Evaluate for Plasmodium parasites.
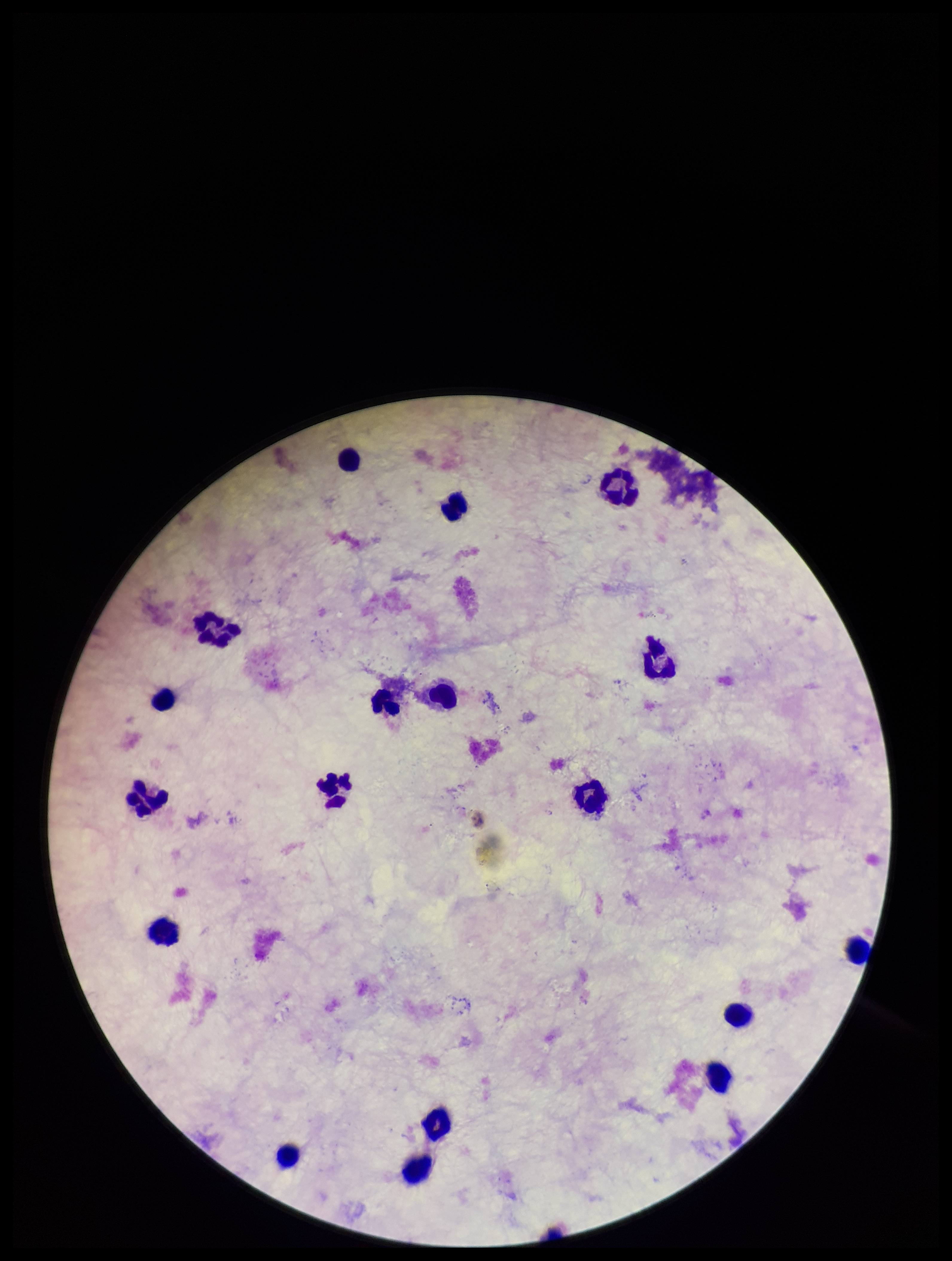

None detected.

preparation = thick smear
leukocyte count = 18
image size = 952×1261 pixels
parasite count = 0
field of view = one from this slide
stain = Giemsa
patient malaria status = negative
capture = smartphone photograph through the microscope eyepiece